Comment on the morphology of the erythrocytes.
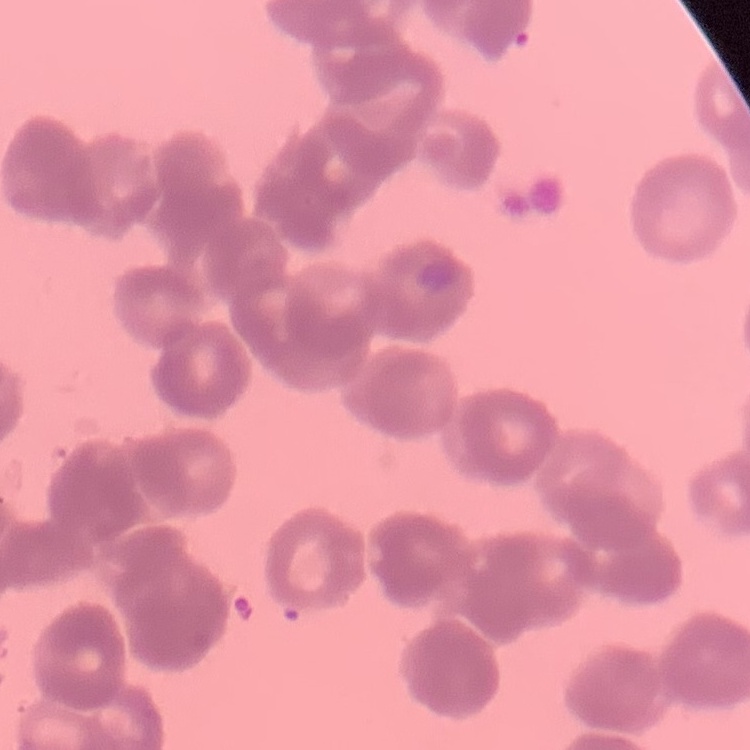

They show rouleaux formation.

image_type: one tile cut from a larger photomicrograph
stain: Field's or Giemsa
preparation: thin peripheral smear